State the blood parasite species.
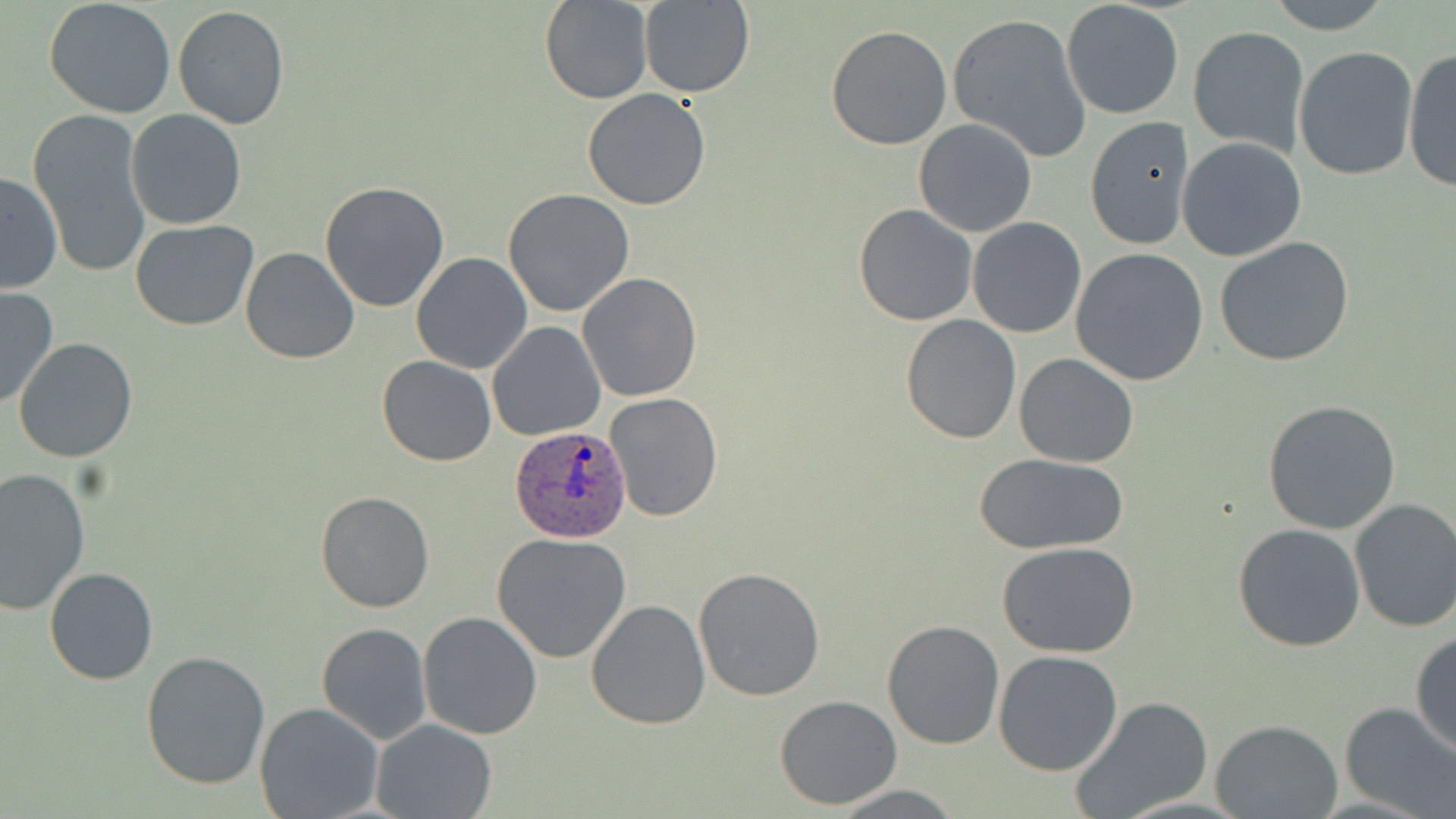
Plasmodium ovale.

stain: May-Grünwald-Giemsa
image_size: 1456×819 pixels
preparation: thin blood smear
uninfected_red_blood_cell_locations: 'approximate bounding boxes as [x1, y1, x2, y2] in pixels: [44, 0, 176, 119], [539, 0, 652, 104], [1262, 0, 1396, 34], [640, 1, 755, 98], [1061, 2, 1184, 118], [172, 6, 291, 129], [946, 11, 1093, 163], [826, 24, 953, 150], [1187, 25, 1309, 155], [1292, 45, 1419, 180], [1401, 46, 1456, 194], [582, 88, 711, 211], [29, 105, 151, 280], [126, 109, 247, 230], [1084, 116, 1196, 249], [914, 119, 1037, 237], [1177, 137, 1307, 262], [0, 173, 63, 296], [319, 181, 450, 313], [503, 188, 635, 318], [853, 203, 979, 326], [131, 218, 258, 331], [967, 218, 1087, 338], [128, 233, 358, 347], [1213, 238, 1357, 368], [241, 247, 360, 365], [1069, 248, 1210, 385], [409, 252, 532, 375], [578, 272, 702, 402], [0, 287, 56, 410], [899, 314, 1020, 443], [487, 321, 605, 441], [13, 338, 139, 464], [1014, 353, 1139, 467], [376, 356, 496, 467], [606, 392, 723, 522], [1262, 398, 1402, 534], [973, 452, 1129, 555], [0, 468, 92, 616], [315, 489, 435, 612], [1349, 497, 1456, 633], [1232, 522, 1365, 652], [491, 532, 633, 663], [998, 543, 1139, 658], [44, 565, 159, 685], [692, 566, 826, 702], [585, 598, 712, 731], [417, 610, 543, 739], [880, 620, 1005, 750], [316, 623, 431, 744], [1410, 628, 1456, 758], [993, 650, 1124, 777], [141, 651, 271, 791], [774, 694, 904, 810], [1068, 696, 1214, 819], [254, 702, 385, 819], [1338, 702, 1456, 817], [369, 718, 497, 819], [1210, 719, 1343, 819], [830, 784, 963, 817]'
magnification: 1000x
modality: light microscopy
field_of_view: single
plasmodium_ovale_infected_red_blood_cell_locations: 'approximate bounding boxes as [x1, y1, x2, y2] in pixels: [509, 424, 632, 542]'